Classify this cell by malaria status.
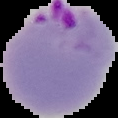

It is parasitized.

Summary:
  - Preparation: thin blood smear
  - Image size: 118×118 pixels
  - Image type: cell region segmented out of the field of view; surrounding area masked to black